Locate every Plasmodium ovale-infected red blood cell.
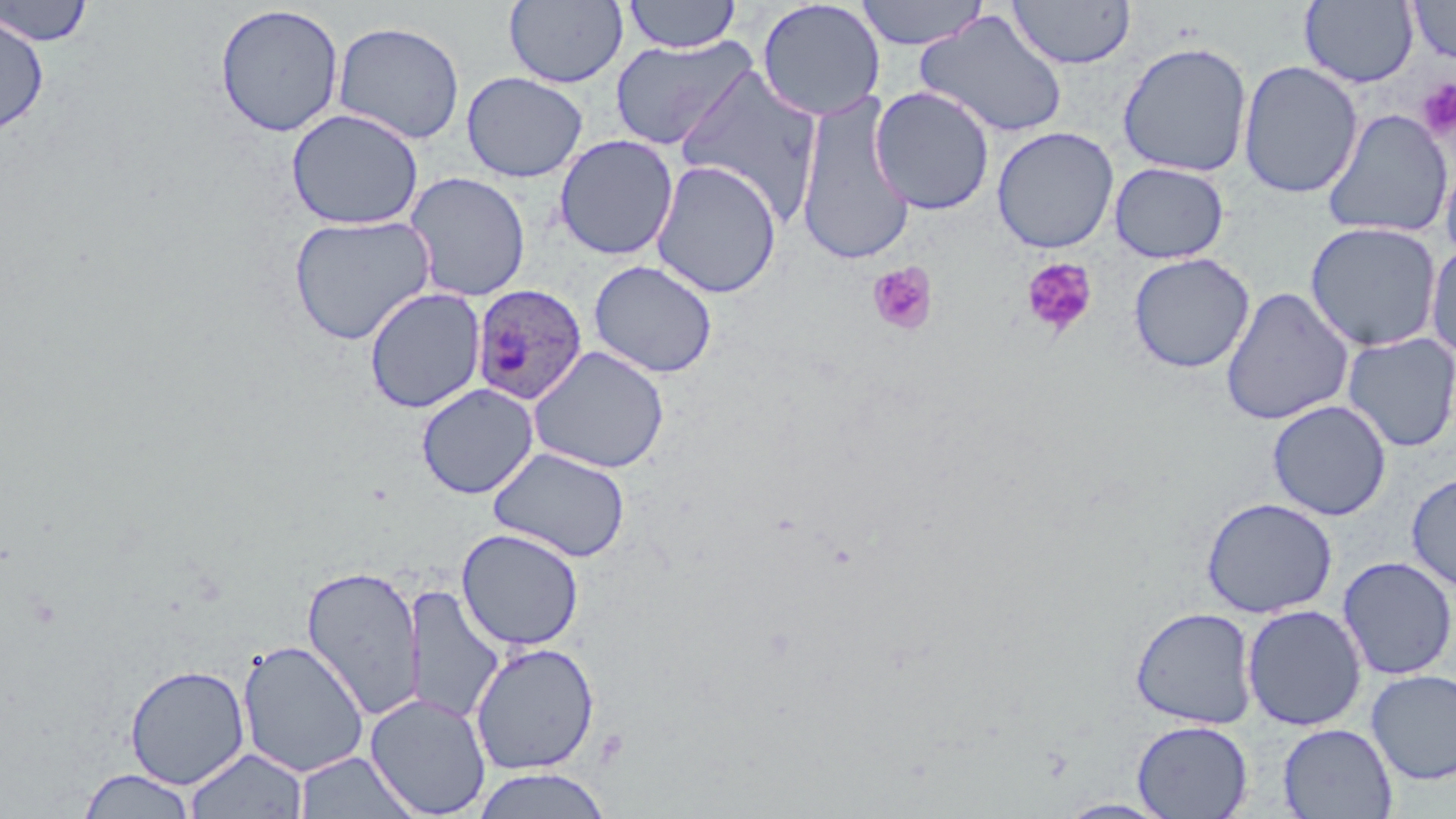
Approximate bounding boxes as [x1, y1, x2, y2] in pixels.
Plasmodium ovale-infected red blood cells: [471, 284, 588, 405].

Summary:
  - Uninfected red blood cell locations: [504, 0, 629, 88], [622, 0, 742, 54], [854, 0, 990, 50], [1407, 0, 1456, 65], [0, 1, 95, 46], [757, 1, 886, 121], [1008, 1, 1136, 69], [1299, 1, 1419, 88], [214, 4, 345, 138], [915, 10, 1069, 139], [0, 11, 50, 135], [333, 21, 465, 145], [609, 35, 759, 151], [1116, 41, 1253, 177], [1238, 60, 1363, 199], [674, 64, 824, 225], [461, 71, 588, 183], [869, 86, 995, 215], [795, 93, 917, 267], [286, 107, 424, 231], [1322, 109, 1453, 238], [991, 126, 1120, 253], [554, 134, 678, 260], [650, 159, 782, 298], [1440, 159, 1456, 268], [1109, 162, 1230, 264], [404, 171, 530, 301], [288, 213, 436, 345], [1305, 221, 1443, 352], [1426, 241, 1456, 362], [1128, 253, 1255, 373], [588, 259, 718, 378], [1220, 286, 1354, 426], [364, 288, 485, 413], [1341, 332, 1456, 452], [528, 345, 670, 474], [416, 383, 539, 499], [1267, 399, 1392, 521], [488, 446, 631, 562], [1406, 473, 1456, 592], [1201, 497, 1338, 618], [457, 528, 584, 651], [1337, 556, 1455, 680], [301, 564, 425, 721], [405, 586, 504, 725], [1242, 604, 1367, 731], [1130, 606, 1258, 729], [237, 639, 370, 777], [470, 641, 600, 775], [124, 664, 250, 789], [1366, 670, 1456, 785], [365, 692, 491, 818], [1132, 719, 1253, 818], [1278, 723, 1398, 819], [185, 748, 309, 819], [295, 751, 419, 819], [77, 768, 198, 818], [470, 768, 613, 818], [1055, 797, 1177, 818]
  - Platelet locations: [1416, 78, 1456, 141], [1021, 257, 1099, 337], [867, 262, 938, 336]
  - Slide-level diagnosis: Plasmodium ovale
  - Image size: 1456×819 pixels
  - Stain: May-Grünwald-Giemsa
  - Field of view: single
  - Magnification: 1000x
  - Preparation: thin blood smear
  - Modality: light microscopy